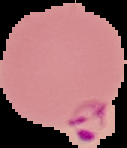

Summary:
  - Image type: segmented cell region with the area outside set to black
  - Preparation: thin blood smear
  - Image size: 127×148 pixels
  - Result: Plasmodium parasites identified